Assess this cell for malaria.
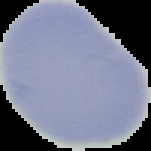

Uninfected.

From a thin blood smear. Segmented cell region on a black background. Image is 151×151 pixels.